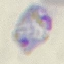 Result: malaria parasites detected. Thin blood smear. Automatically extracted cell patch, resized to 64 × 64 pixels. Acquired by smartphone through the microscope eyepiece. Giemsa stain.